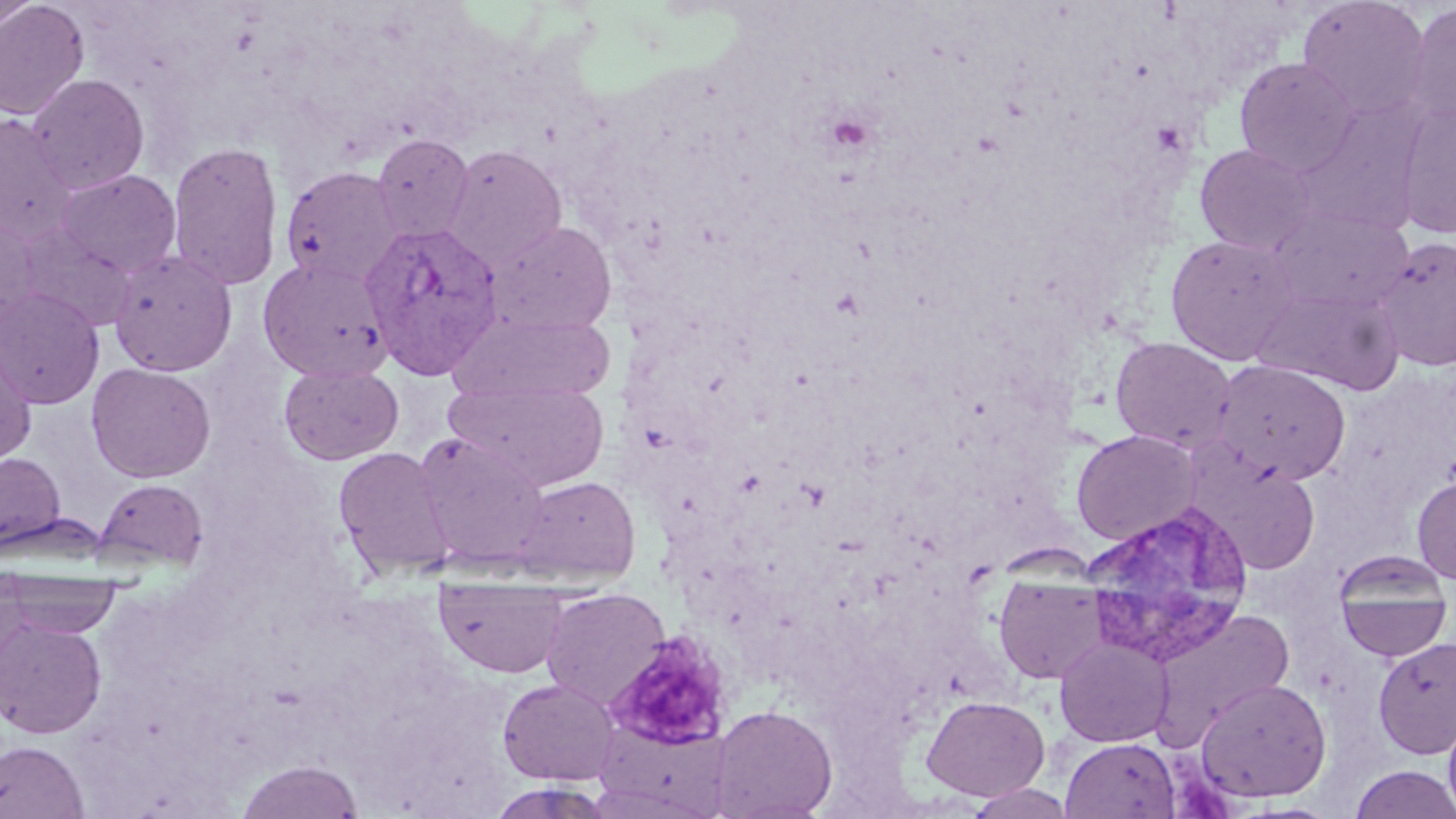

Summary:
  - Coordinate format: approximate bounding boxes as (x1,y1)-(x2,y2) corner pairs in pixels
  - Uninfected red blood cell locations: (0,0)-(41,30), (1296,0)-(1431,121), (0,1)-(90,120), (1404,4)-(1456,128), (1234,57)-(1359,176), (26,74)-(150,194), (1293,101)-(1426,237), (1395,102)-(1456,239), (0,114)-(77,243), (371,133)-(474,244), (167,139)-(285,291), (1195,144)-(1318,256), (441,145)-(567,271), (280,165)-(405,287), (55,168)-(182,278), (1269,206)-(1414,315), (0,218)-(41,331), (489,220)-(618,336), (13,221)-(137,330), (1164,233)-(1301,365), (1370,236)-(1456,372), (108,249)-(237,376), (258,257)-(392,381), (1255,284)-(1404,395), (0,288)-(104,409), (453,310)-(617,405), (1110,337)-(1237,453), (1,338)-(37,466), (1211,360)-(1352,486), (86,362)-(216,483), (278,363)-(404,465), (446,377)-(608,492), (1071,429)-(1203,545), (413,432)-(553,570), (333,446)-(454,579), (0,452)-(67,551), (1201,464)-(1321,575), (1413,475)-(1456,584), (513,476)-(640,584), (94,479)-(208,571), (1333,552)-(1454,662), (994,572)-(1111,685), (3,574)-(122,639), (435,582)-(570,678), (542,587)-(672,711), (1146,609)-(1295,748), (0,614)-(107,738), (1373,634)-(1456,760), (1055,635)-(1175,747), (1195,677)-(1332,802), (497,678)-(621,785), (921,694)-(1049,801), (710,704)-(838,818), (1443,708)-(1456,818), (595,721)-(733,816), (1061,737)-(1181,818), (0,740)-(89,818), (235,759)-(365,818), (1350,765)-(1456,818), (963,783)-(1077,819)
  - Plasmodium vivax-infected red blood cell locations: (360,221)-(503,379), (1081,502)-(1256,667)
  - Platelet locations: (823,110)-(877,157), (1151,120)-(1189,156)
  - Slide-level diagnosis: Plasmodium vivax
  - Image size: 1456×819 pixels
  - Stain: May-Grünwald-Giemsa
  - Modality: light microscopy
  - Field of view: single
  - Preparation: thin blood smear
  - Magnification: 1000x